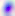

400x magnification. Micrograph. Toxoplasma gondii is seen.